Report the malaria status of this cell.
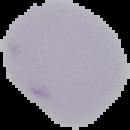
Uninfected.

preparation = thin blood film
image type = segmented cell region with the area outside set to black
image size = 130×130 pixels